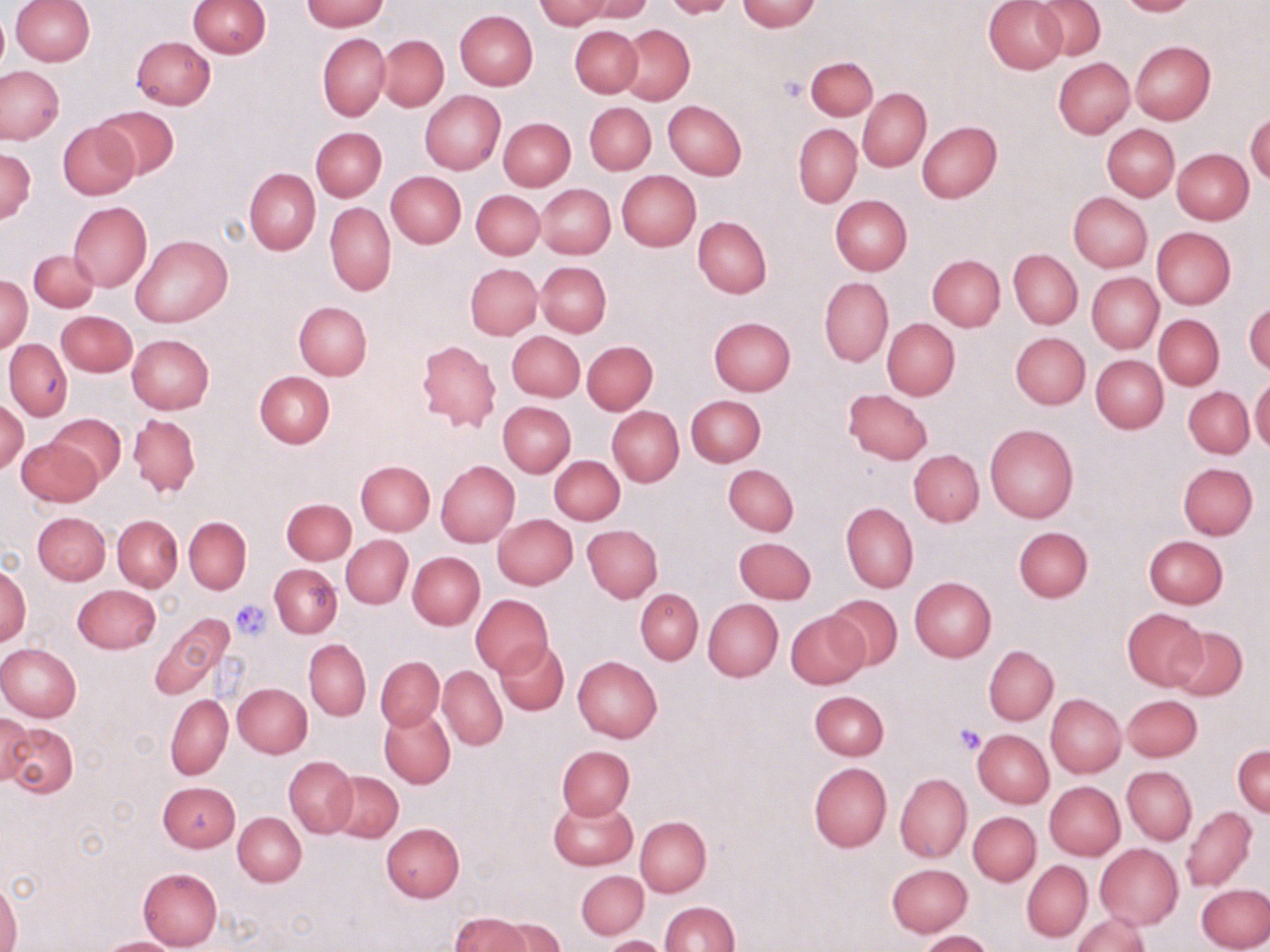

slide-level diagnosis = no evidence of blood parasites
preparation = thin blood smear
field of view = single
stain = May-Grünwald-Giemsa
platelet locations = approximate bounding boxes as (x1, y1, x2, y2) in pixels: (779, 76, 808, 102), (229, 599, 272, 640), (954, 725, 986, 755)
magnification = 1000x
modality = light microscopy
uninfected red blood cell locations = approximate bounding boxes as (x1, y1, x2, y2) in pixels: (189, 0, 270, 57), (302, 0, 388, 31), (537, 0, 615, 29), (578, 0, 654, 23), (661, 0, 740, 19), (736, 0, 822, 31), (984, 0, 1067, 74), (1114, 0, 1200, 16), (9, 1, 95, 65), (1033, 1, 1106, 59), (0, 8, 8, 79), (455, 10, 537, 91), (570, 25, 642, 97), (618, 25, 694, 103), (318, 32, 390, 121), (378, 35, 448, 111), (131, 37, 216, 110), (1130, 42, 1215, 125), (804, 56, 876, 121), (1053, 58, 1133, 137), (0, 65, 65, 145), (858, 88, 931, 171), (420, 90, 506, 174), (664, 100, 746, 179), (585, 102, 655, 174), (94, 104, 180, 180), (1246, 112, 1270, 184), (499, 117, 575, 190), (58, 120, 140, 201), (916, 121, 1001, 203), (794, 123, 861, 207), (1102, 125, 1178, 201), (311, 127, 387, 202), (1, 148, 36, 224), (1171, 148, 1253, 224), (244, 168, 320, 255), (386, 171, 466, 248), (617, 171, 701, 250), (537, 184, 615, 258), (472, 190, 545, 260), (1069, 193, 1152, 272), (830, 194, 912, 275), (68, 202, 151, 292), (325, 202, 395, 295), (694, 216, 772, 298), (1152, 227, 1236, 309), (132, 235, 232, 328), (28, 249, 101, 312), (1009, 249, 1081, 329), (927, 255, 1004, 331), (536, 261, 610, 337), (465, 263, 542, 340), (1087, 272, 1162, 351), (0, 275, 31, 353), (820, 276, 892, 367), (294, 301, 371, 380), (1245, 301, 1270, 376), (58, 311, 137, 376), (1154, 314, 1223, 390), (708, 316, 796, 394), (883, 319, 960, 400), (507, 331, 584, 402), (1011, 333, 1090, 409), (127, 334, 213, 414), (4, 339, 72, 421), (417, 340, 501, 433), (582, 341, 657, 413), (1091, 354, 1169, 433), (254, 371, 334, 447), (1249, 377, 1269, 454), (1184, 386, 1253, 457), (844, 388, 932, 464), (686, 395, 765, 467), (0, 399, 28, 473), (497, 402, 575, 476), (608, 407, 683, 486), (51, 413, 126, 486), (128, 414, 200, 499), (985, 423, 1078, 522), (17, 436, 103, 507), (910, 450, 984, 526), (550, 455, 624, 525), (355, 460, 434, 535), (436, 460, 519, 547), (1178, 463, 1257, 540), (723, 464, 798, 536), (281, 498, 357, 564), (841, 502, 918, 592), (33, 512, 110, 584), (493, 514, 577, 589), (113, 515, 183, 591), (184, 516, 251, 594), (583, 525, 662, 602), (1012, 526, 1093, 603), (342, 535, 413, 608), (1144, 535, 1228, 607), (735, 536, 816, 602), (409, 552, 484, 629), (270, 564, 342, 637), (0, 567, 31, 644), (910, 578, 996, 661), (73, 585, 161, 653), (636, 588, 703, 664), (471, 595, 552, 676), (825, 595, 902, 670), (703, 599, 782, 681), (1122, 607, 1207, 690), (786, 611, 867, 688), (148, 615, 233, 698), (1170, 626, 1247, 700), (305, 639, 371, 721), (497, 639, 569, 715), (0, 644, 81, 722), (984, 646, 1057, 725), (376, 656, 444, 730), (573, 656, 663, 741), (438, 667, 507, 750), (234, 683, 313, 757), (809, 690, 889, 759), (1046, 693, 1125, 778), (166, 695, 232, 778), (1124, 695, 1202, 761), (379, 707, 456, 788), (0, 712, 34, 788), (5, 722, 78, 797), (973, 729, 1053, 808), (557, 745, 634, 819), (1233, 745, 1270, 817), (285, 756, 357, 837), (809, 762, 892, 852), (1122, 766, 1197, 844), (329, 770, 402, 842), (894, 773, 971, 862), (158, 781, 239, 851), (1043, 781, 1125, 860), (548, 797, 636, 870), (1181, 806, 1256, 891), (967, 811, 1041, 885), (234, 813, 305, 886), (635, 815, 711, 897), (381, 822, 465, 901), (1095, 843, 1183, 929), (1021, 859, 1092, 942), (887, 863, 972, 936), (137, 867, 222, 950), (577, 871, 647, 939), (0, 881, 22, 952), (1197, 882, 1270, 952), (660, 901, 739, 952), (1071, 912, 1151, 952), (449, 913, 537, 952), (495, 918, 567, 951), (918, 930, 993, 952), (602, 935, 672, 952), (96, 937, 186, 952)
image size = 1270×952 pixels